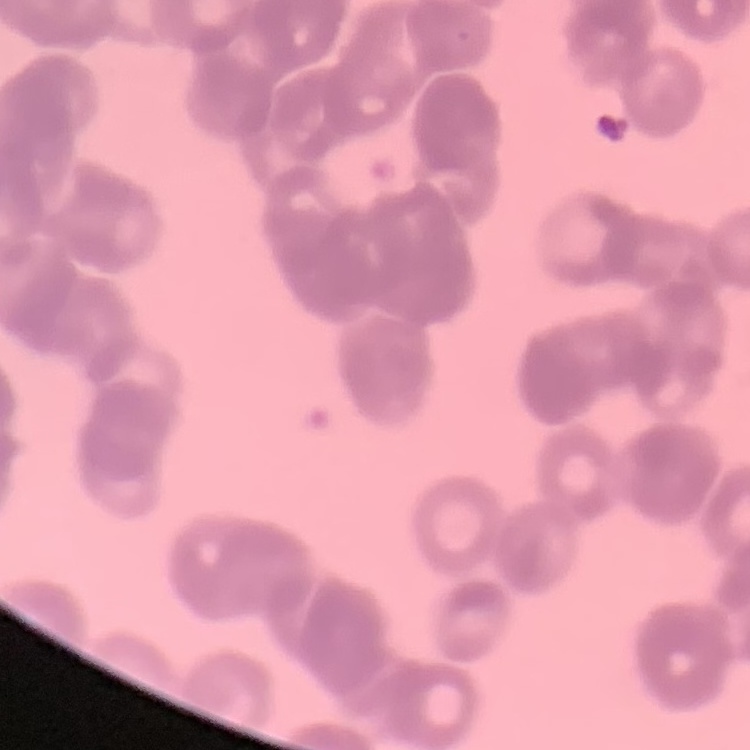
The erythrocytes show rouleaux formation. Field's or Giemsa stain. Square crop of a larger photomicrograph. Thin blood smear.